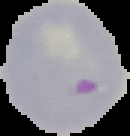

preparation = thin blood smear
malaria status = parasitized
image size = 130×136 pixels
image type = segmented cell region on a black background